Give the position of every malaria parasite and every leukocyte.
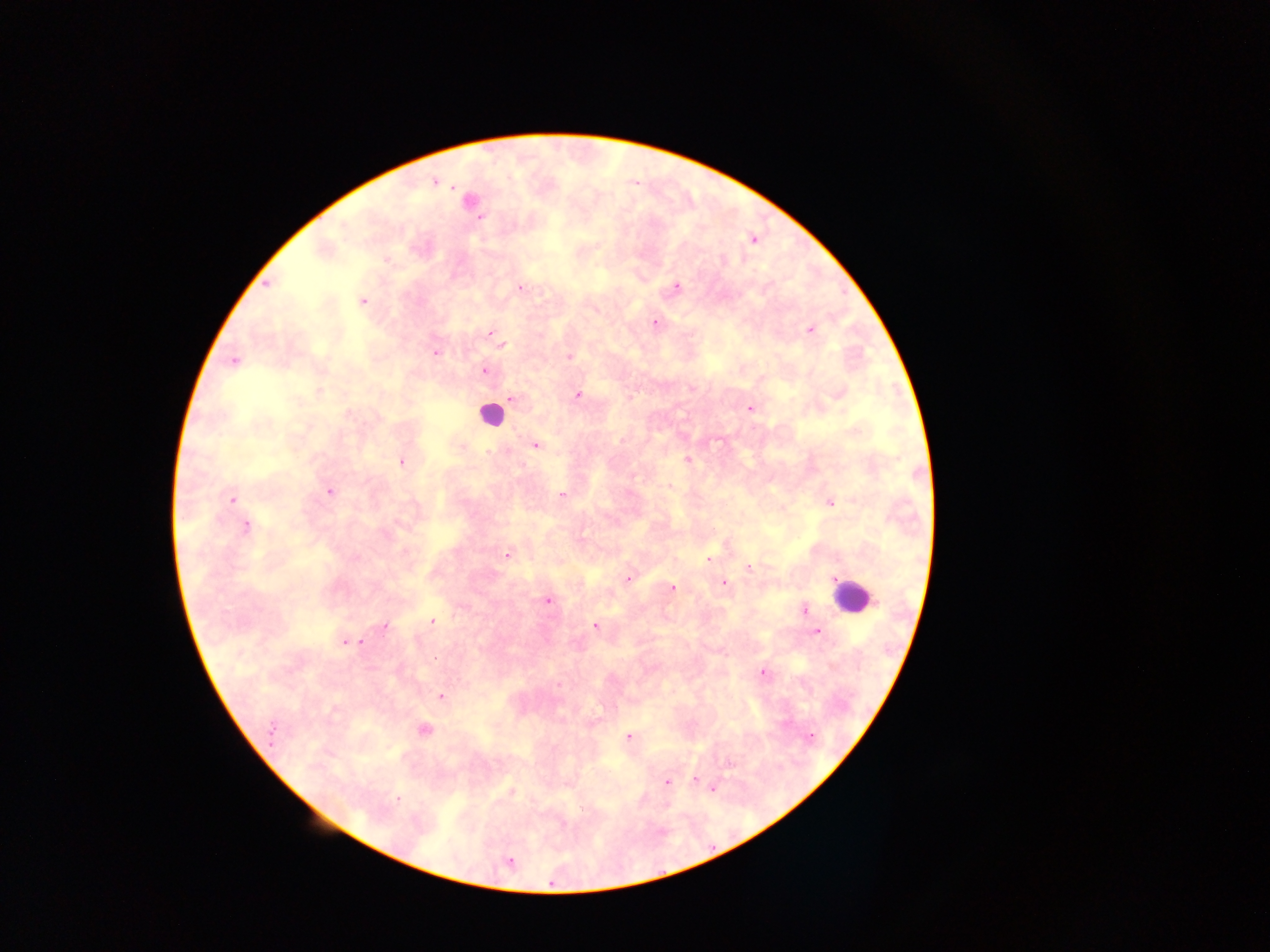
Approximate centers as x y in pixels.
Malaria parasites: 433 181; 469 201; 479 218; 753 239; 322 248; 386 259; 268 284; 520 288; 676 288; 362 301; 655 322; 810 329; 489 333; 503 345; 435 353; 569 356; 234 361; 484 370; 318 392; 838 392; 577 395; 511 399; 749 407; 535 445; 686 459; 401 462; 669 487; 330 491; 561 495; 231 499; 830 502; 244 526; 508 554; 709 558; 749 568; 629 578; 723 583; 672 589; 546 600; 804 609; 432 621; 595 625; 383 626; 816 631; 345 642; 762 673; 559 685; 440 695; 423 730; 809 736; 628 737; 694 781; 667 782; 711 786; 510 791; 397 798; 509 862.
Leukocytes: 489 415; 851 596.

preparation = thick blood smear
image size = 1270×952 pixels
field of view = single
country = Ghana
capture = mobile-phone photograph through a microscope